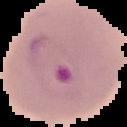
From a thin blood smear. Result: malaria parasites identified. Segmented cell region on a black background. Image is 127×127 pixels.